Assess this cell for malaria.
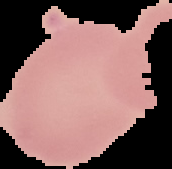
Uninfected.

Summary:
  - Image size: 172×169 pixels
  - Image type: segmented cell region on a black background
  - Preparation: thin blood smear